Identify the blood parasite species.
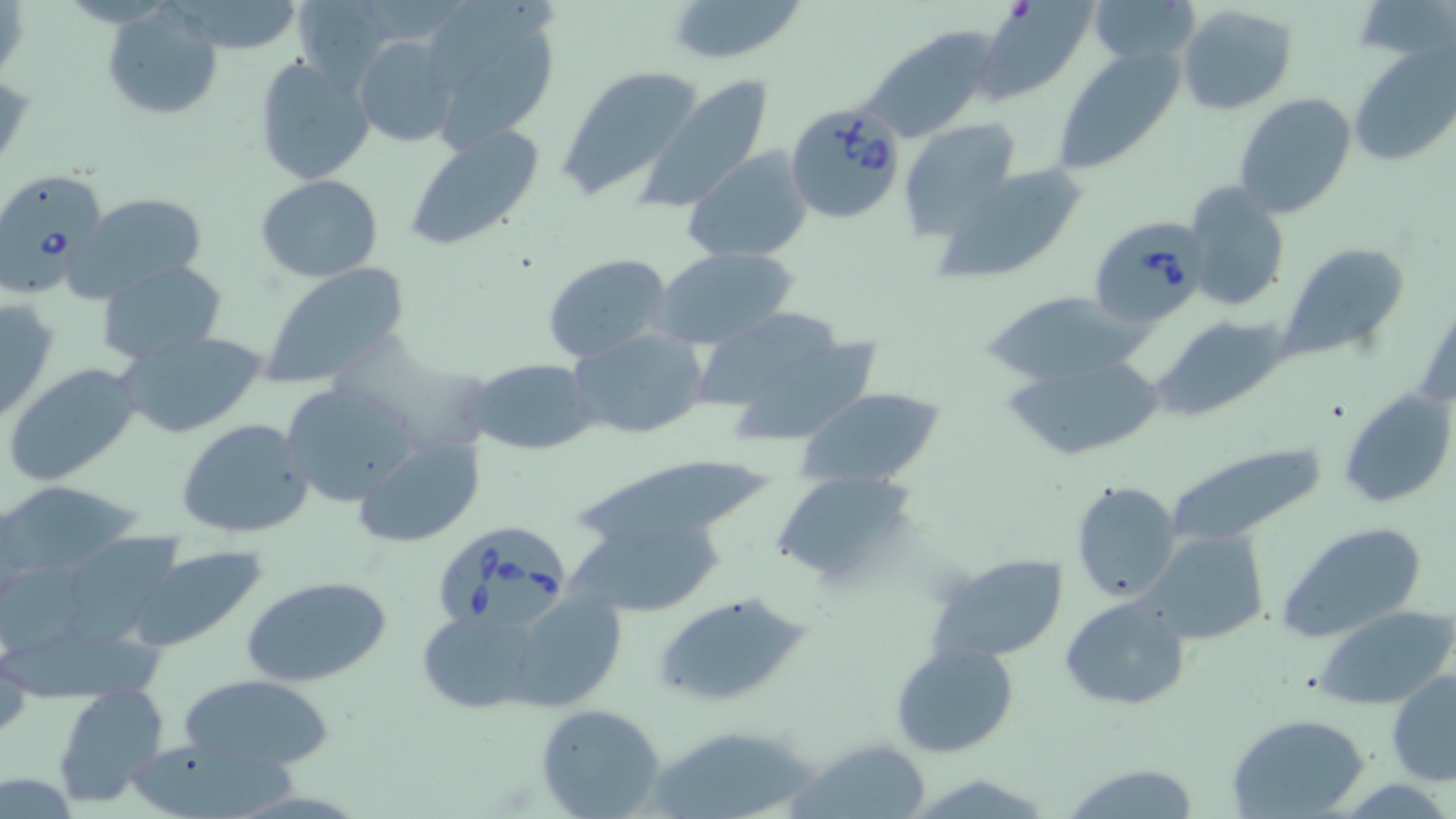
Babesia divergens.

Summary:
  - Coordinate format: approximate bounding boxes as (x1, y1, x2, y2) in pixels
  - Babesia divergens-infected red blood cell locations: (786, 103, 907, 224), (0, 175, 108, 301), (1091, 215, 1208, 329), (436, 512, 568, 630)
  - Uninfected red blood cell locations: (421, 0, 561, 149), (664, 0, 808, 66), (1087, 0, 1201, 65), (1175, 3, 1298, 115), (976, 4, 1093, 102), (103, 7, 222, 121), (859, 26, 1001, 142), (352, 36, 461, 148), (1351, 45, 1456, 168), (1052, 47, 1186, 175), (254, 55, 374, 185), (555, 65, 705, 198), (635, 74, 776, 214), (1232, 92, 1358, 219), (898, 119, 1022, 239), (402, 123, 546, 250), (683, 145, 815, 265), (931, 162, 1091, 283), (257, 175, 383, 282), (1181, 182, 1292, 312), (67, 192, 210, 299), (1281, 243, 1413, 360), (652, 246, 800, 350), (542, 252, 675, 365), (97, 260, 228, 365), (259, 263, 413, 390), (980, 290, 1146, 386), (0, 296, 61, 425), (1152, 315, 1289, 419), (699, 317, 885, 445), (569, 328, 709, 442), (116, 331, 268, 439), (1004, 354, 1162, 462), (464, 358, 599, 455), (3, 361, 143, 487), (278, 379, 415, 506), (1337, 384, 1456, 512), (793, 388, 946, 489), (175, 417, 314, 539), (355, 437, 485, 548), (1159, 437, 1331, 550), (576, 459, 774, 547), (771, 469, 921, 588), (2, 477, 147, 582), (1069, 479, 1183, 603), (1275, 519, 1431, 642), (569, 527, 728, 613), (1137, 531, 1269, 646), (56, 532, 190, 641), (126, 546, 270, 654), (927, 552, 1068, 665), (243, 575, 394, 689), (503, 591, 627, 710), (651, 591, 813, 708), (1061, 596, 1191, 711), (1312, 605, 1455, 711), (416, 608, 548, 712), (0, 634, 181, 703), (890, 640, 1021, 757), (1387, 669, 1456, 787), (177, 671, 337, 775), (52, 685, 169, 808), (536, 704, 668, 818), (1227, 713, 1371, 818), (790, 737, 933, 819), (125, 742, 316, 811), (1058, 763, 1204, 819)
  - Magnification: 1000x
  - Image size: 1456×819 pixels
  - Preparation: thin blood film
  - Modality: optical microscopy
  - Field of view: one of a larger specimen
  - Stain: May-Grünwald-Giemsa